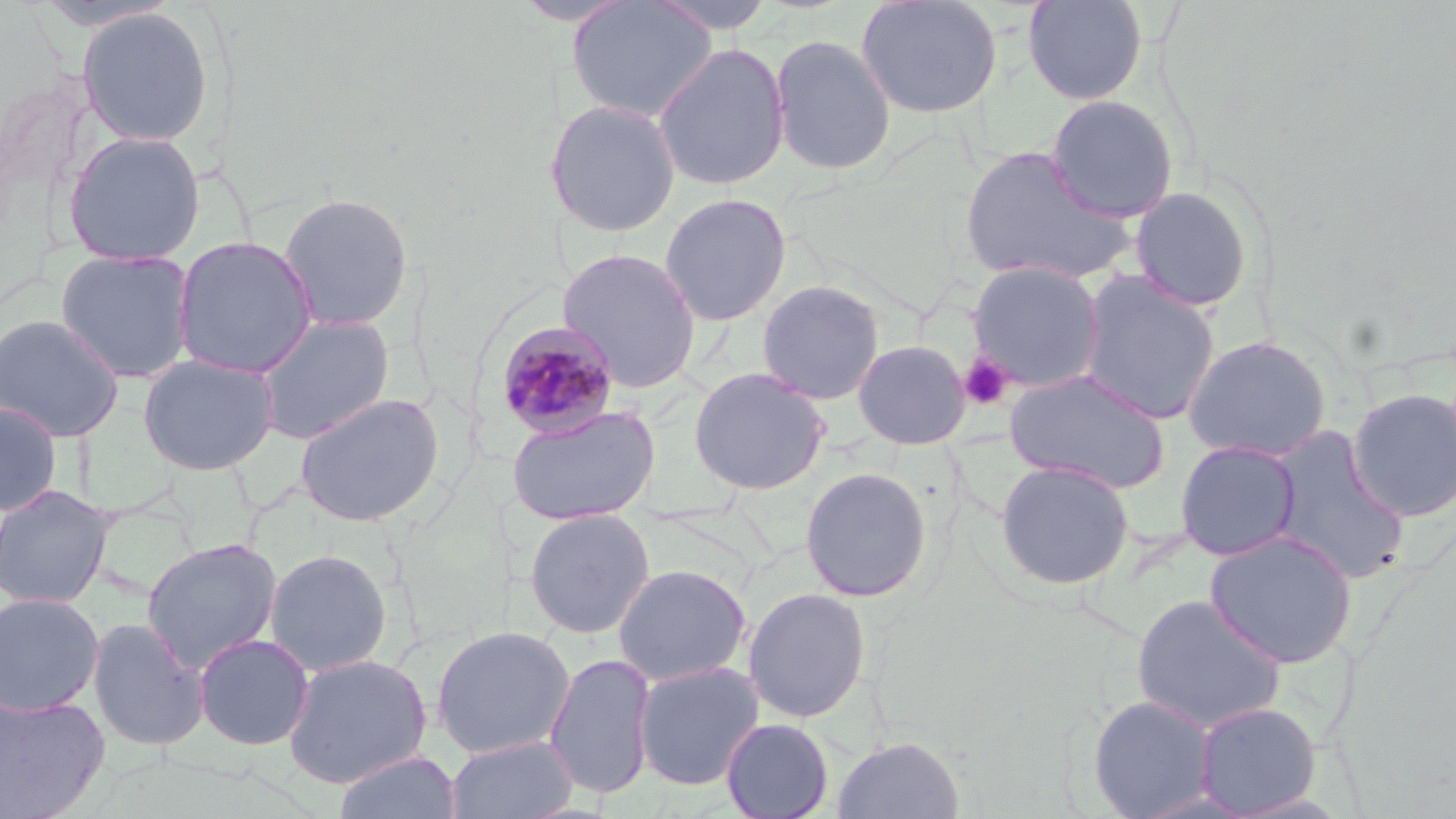
slide-level diagnosis = Plasmodium malariae
preparation = thin blood film
field of view = one of a larger specimen
image size = 1456×819 pixels
modality = optical microscopy
Plasmodium malariae-infected red blood cell locations = approximate bounding boxes as [x1, y1, x2, y2] in pixels: [492, 319, 622, 439]
magnification = 1000x
uninfected red blood cell locations = approximate bounding boxes as [x1, y1, x2, y2] in pixels: [648, 0, 779, 34], [856, 0, 1002, 119], [1022, 0, 1148, 106], [565, 1, 718, 123], [76, 7, 215, 147], [768, 33, 896, 176], [653, 43, 790, 191], [1045, 94, 1180, 223], [543, 99, 682, 238], [62, 130, 206, 266], [958, 145, 1135, 288], [1129, 186, 1254, 313], [278, 192, 414, 332], [659, 193, 792, 326], [172, 235, 318, 379], [557, 247, 703, 393], [54, 248, 196, 383], [966, 260, 1106, 393], [1077, 270, 1221, 425], [755, 279, 886, 405], [0, 313, 125, 442], [255, 313, 395, 444], [1182, 334, 1332, 462], [852, 339, 971, 450], [138, 353, 279, 475], [689, 366, 830, 496], [1003, 368, 1170, 493], [1346, 387, 1456, 522], [293, 391, 446, 527], [0, 400, 62, 516], [506, 405, 661, 525], [1263, 427, 1411, 586], [1174, 439, 1302, 561], [994, 458, 1135, 591], [800, 466, 932, 602], [0, 485, 117, 609], [523, 508, 655, 639], [1204, 530, 1358, 668], [141, 537, 282, 673], [264, 548, 393, 677], [613, 563, 752, 686], [742, 586, 872, 723], [0, 592, 104, 716], [1131, 593, 1287, 733], [87, 617, 210, 751], [431, 625, 575, 758], [193, 633, 314, 750], [545, 652, 656, 800], [282, 653, 432, 789], [633, 660, 765, 791], [0, 693, 110, 818], [1087, 694, 1218, 818], [1192, 701, 1322, 816], [720, 718, 834, 819], [445, 734, 578, 819], [831, 736, 965, 819], [332, 750, 462, 819]
platelet locations = approximate bounding boxes as [x1, y1, x2, y2] in pixels: [958, 353, 1017, 410]
stain = May-Grünwald-Giemsa